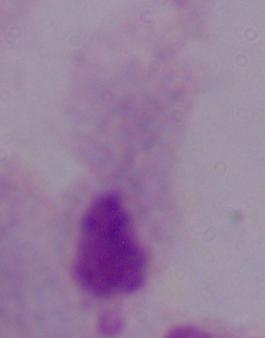

modality = micrograph
identification = trichomonad
magnification = 1000x